Name the parasite shown.
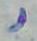

This is Toxoplasma gondii.

Photomicrograph. 1000x magnification.